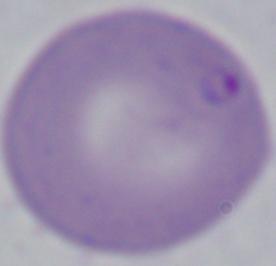
identification = Babesia
magnification = 1000x
modality = micrograph